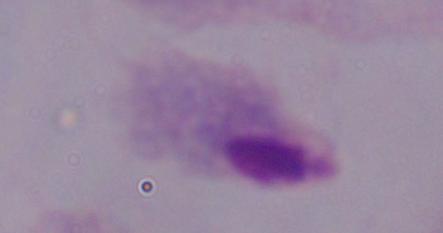

Summary:
  - Magnification: 1000x
  - Identification: trichomonad
  - Modality: photomicrograph